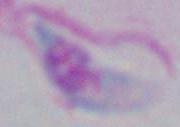

Summary:
  - Modality: micrograph
  - Magnification: 1000x
  - Identification: Toxoplasma gondii